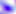
Summary:
  - Modality: micrograph
  - Identification: Toxoplasma gondii
  - Magnification: 400x